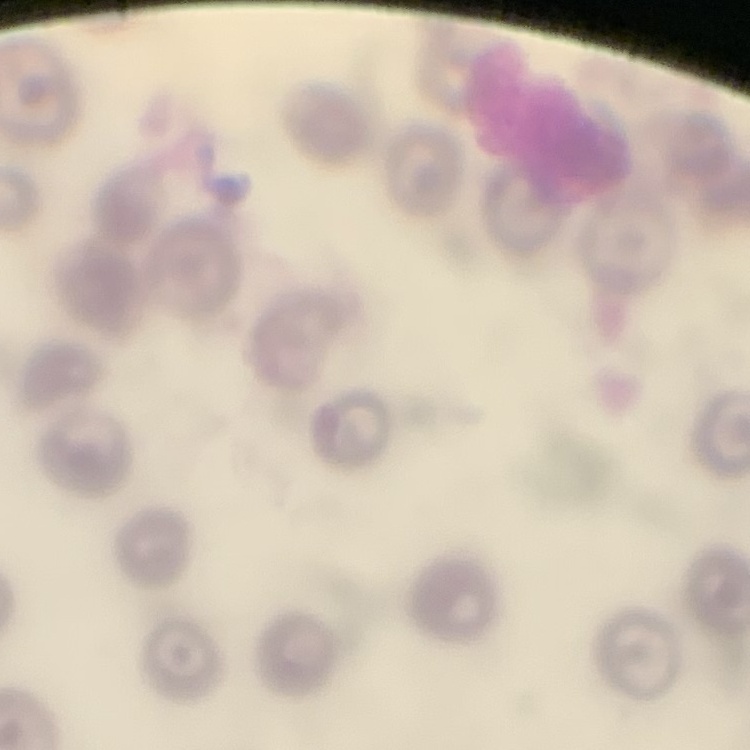

The erythrocytes show no rouleaux formation. Thin blood film. Field's or Giemsa stain. One tile cut from a larger photomicrograph.